Outline each uninfected red blood cell.
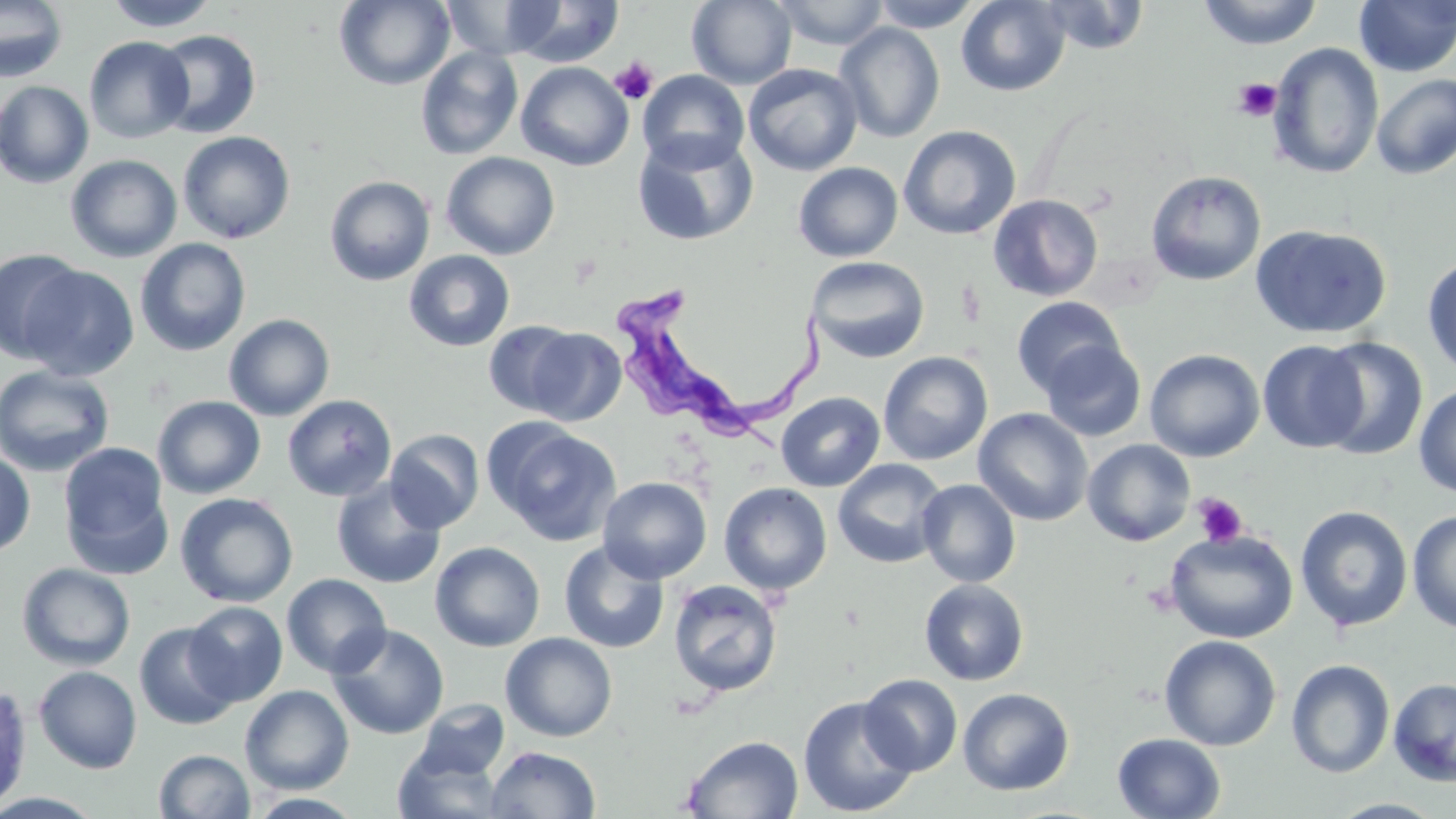
Approximate bounding boxes as [x1, y1, x2, y2] in pixels.
Uninfected red blood cells: [0, 0, 68, 83], [103, 0, 220, 32], [334, 0, 455, 90], [439, 0, 563, 58], [687, 0, 798, 89], [771, 0, 891, 50], [869, 0, 984, 32], [956, 0, 1070, 96], [1197, 0, 1324, 49], [1355, 0, 1455, 77], [502, 1, 625, 67], [1038, 1, 1149, 55], [834, 23, 945, 143], [151, 29, 261, 139], [83, 36, 194, 143], [1268, 43, 1384, 179], [415, 47, 524, 160], [516, 62, 634, 171], [743, 63, 863, 176], [638, 70, 750, 172], [1371, 73, 1456, 180], [0, 80, 94, 189], [898, 125, 1021, 240], [177, 130, 296, 244], [633, 132, 758, 246], [441, 152, 560, 260], [65, 154, 183, 262], [793, 162, 903, 262], [1146, 170, 1266, 286], [324, 176, 435, 286], [988, 194, 1103, 302], [1251, 224, 1392, 339], [135, 238, 251, 357], [0, 248, 89, 363], [404, 250, 516, 352], [1422, 255, 1456, 379], [807, 256, 930, 364], [20, 264, 139, 381], [1012, 296, 1126, 397], [224, 313, 335, 421], [483, 320, 583, 416], [524, 327, 626, 426], [1314, 338, 1429, 460], [1257, 340, 1368, 453], [1040, 341, 1147, 441], [1144, 349, 1265, 462], [878, 351, 993, 466], [0, 365, 116, 477], [1414, 383, 1456, 497], [776, 391, 885, 492], [282, 394, 397, 501], [153, 395, 266, 499], [973, 408, 1093, 526], [488, 421, 622, 546], [385, 429, 484, 534], [1082, 439, 1196, 546], [58, 441, 174, 577], [0, 449, 36, 558], [832, 458, 949, 569], [598, 476, 712, 584], [330, 478, 446, 589], [917, 479, 1021, 588], [719, 482, 832, 596], [175, 492, 298, 608], [1295, 505, 1413, 632], [1407, 509, 1456, 633], [1164, 529, 1299, 644], [559, 539, 670, 653], [429, 541, 545, 652], [17, 562, 136, 671], [281, 573, 392, 677], [668, 579, 783, 697], [919, 579, 1029, 686], [184, 601, 288, 706], [134, 621, 240, 730], [328, 623, 449, 740], [500, 632, 618, 742], [1159, 634, 1281, 751], [1286, 659, 1395, 778], [33, 665, 142, 774], [859, 673, 963, 776], [1387, 677, 1456, 787], [0, 679, 33, 811], [240, 684, 355, 795], [958, 688, 1074, 796], [798, 696, 917, 817], [410, 699, 511, 783], [1112, 732, 1226, 818], [682, 735, 804, 818], [392, 741, 506, 819], [485, 746, 601, 819], [153, 749, 255, 819], [244, 792, 367, 818], [1327, 798, 1448, 818].

Summary:
  - Trypanosoma brucei locations: [615, 278, 843, 454]
  - Platelet locations: [610, 58, 658, 105], [1233, 78, 1282, 121], [1192, 493, 1248, 547]
  - Slide-level diagnosis: Trypanosoma brucei
  - Preparation: thin blood smear
  - Stain: May-Grünwald-Giemsa
  - Field of view: single
  - Modality: light microscopy
  - Magnification: 1000x
  - Image size: 1456×819 pixels